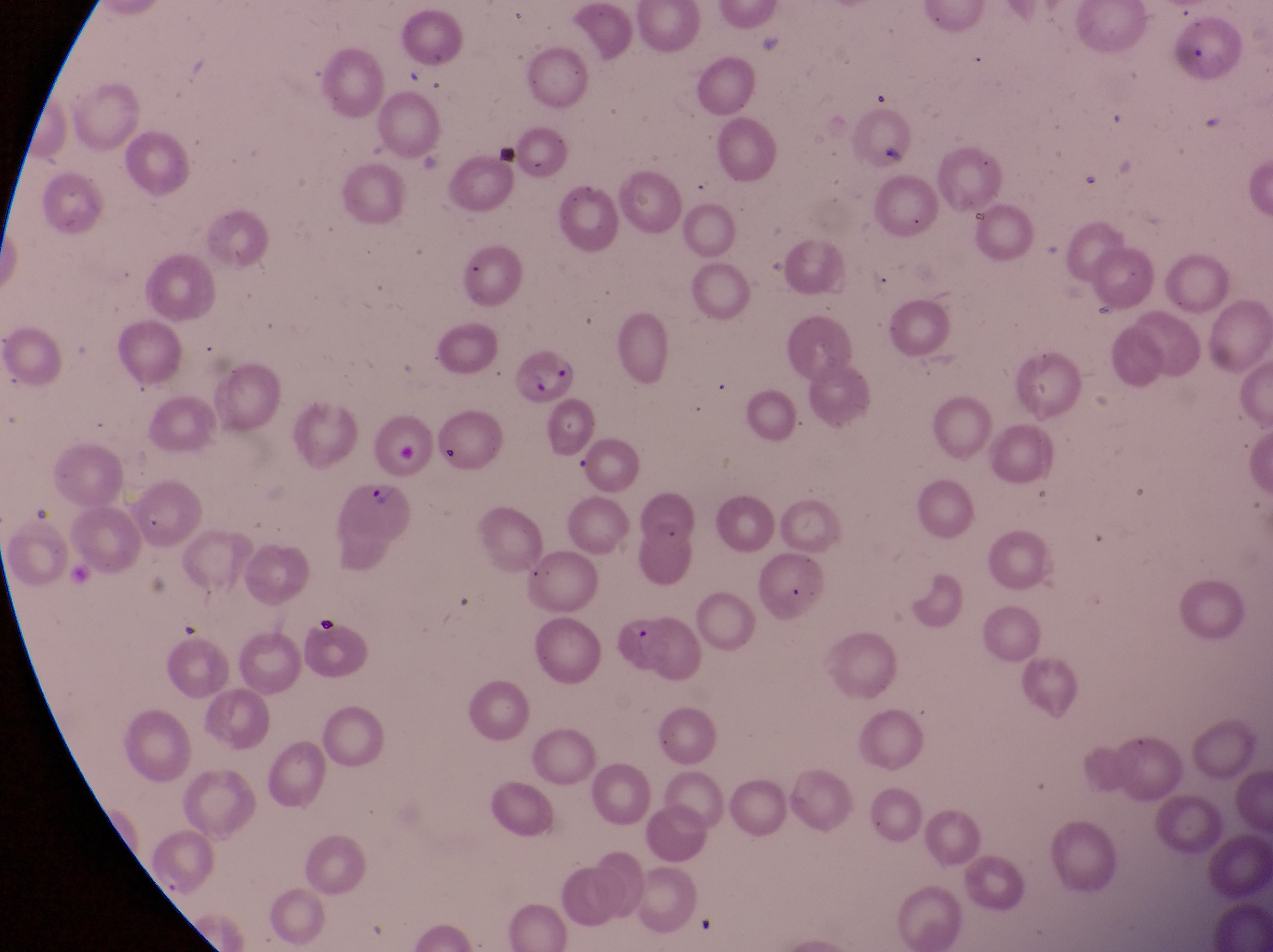

Approximate bounding boxes as {left, top, right, bottom} in pixels.
Summary:
  - Parasitised red blood cell locations: {509, 347, 579, 407}, {626, 475, 698, 553}, {335, 480, 413, 572}
  - Artifact (platelet-like body, stain precipitate, or debris) locations: {437, 434, 465, 471}, {310, 614, 347, 644}
  - Field of view: single
  - Preparation: thin blood smear
  - Country: Uganda
  - Capture: smartphone photograph through the eyepiece of an Olympus CX-23 microscope
  - Image size: 1273×952 pixels
  - Magnification: 1000x